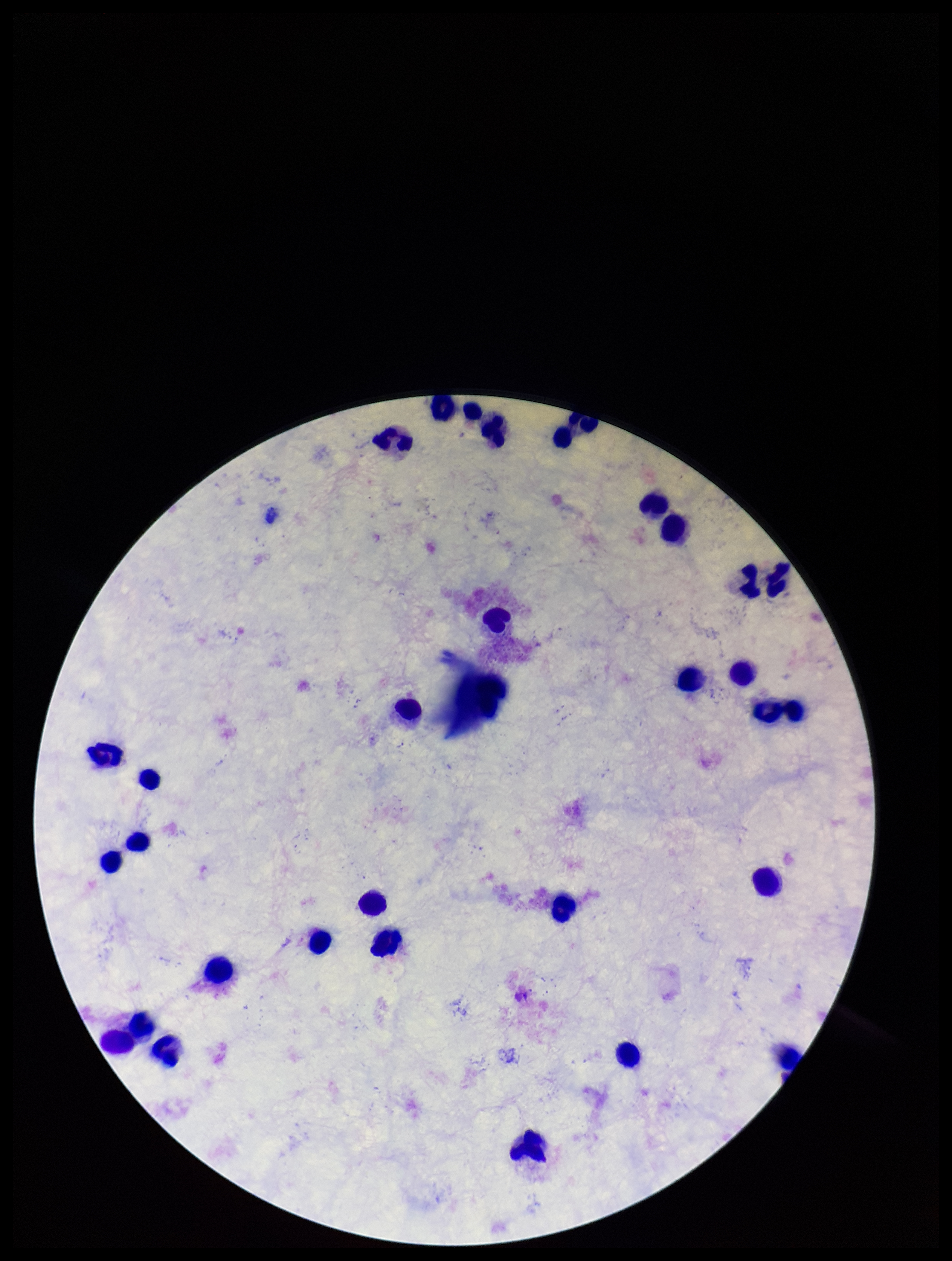
{
  "patient_malaria_status": "negative",
  "preparation": "thick smear",
  "parasite_count": 0,
  "plasmodium_parasites": "none seen",
  "stain": "Giemsa",
  "leukocyte_count": 33,
  "field_of_view": "one from this slide",
  "image_size": "952×1261 pixels",
  "capture": "smartphone photograph through the microscope eyepiece"
}